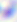
Summary:
  - Magnification: 400x
  - Identification: Toxoplasma gondii
  - Modality: photomicrograph